Report the malaria status of this cell.
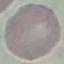

It is uninfected.

Thin blood film. Cell patch, automatically extracted from a larger field of view and resized to 64 × 64 pixels. Acquired by smartphone through the microscope eyepiece. Giemsa stain.